Assess this cell for malaria.
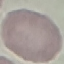

It is uninfected.

preparation = thin smear
capture = smartphone camera at the microscope eyepiece
stain = Giemsa
image type = cell patch, automatically extracted from a larger field of view and resized to 64 × 64 pixels